Report the malaria status of this cell.
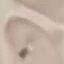

It is uninfected.

stain = Giemsa
capture = smartphone through the microscope eyepiece
image type = cell patch, automatically extracted from a larger field of view and resized to 64 × 64 pixels
preparation = thin smear